Point out each malaria parasite.
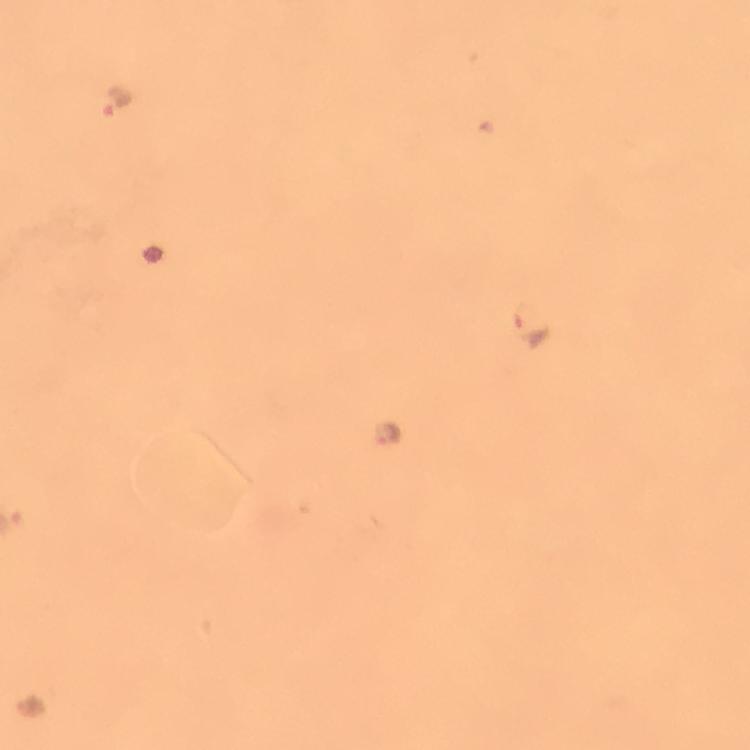
Approximate object centers, in pixels from the top-left corner.
Malaria parasites: (x=117, y=102), (x=532, y=328), (x=387, y=434).

cropped_from: a single field of view
capture: smartphone photograph through a microscope
context: from a malaria diagnostic workup
magnification: 100x
preparation: thick blood smear
image_size: 750×750 pixels
stain: Giemsa
immersion_oil: used